Locate malaria parasites and identify their life-cycle stages.
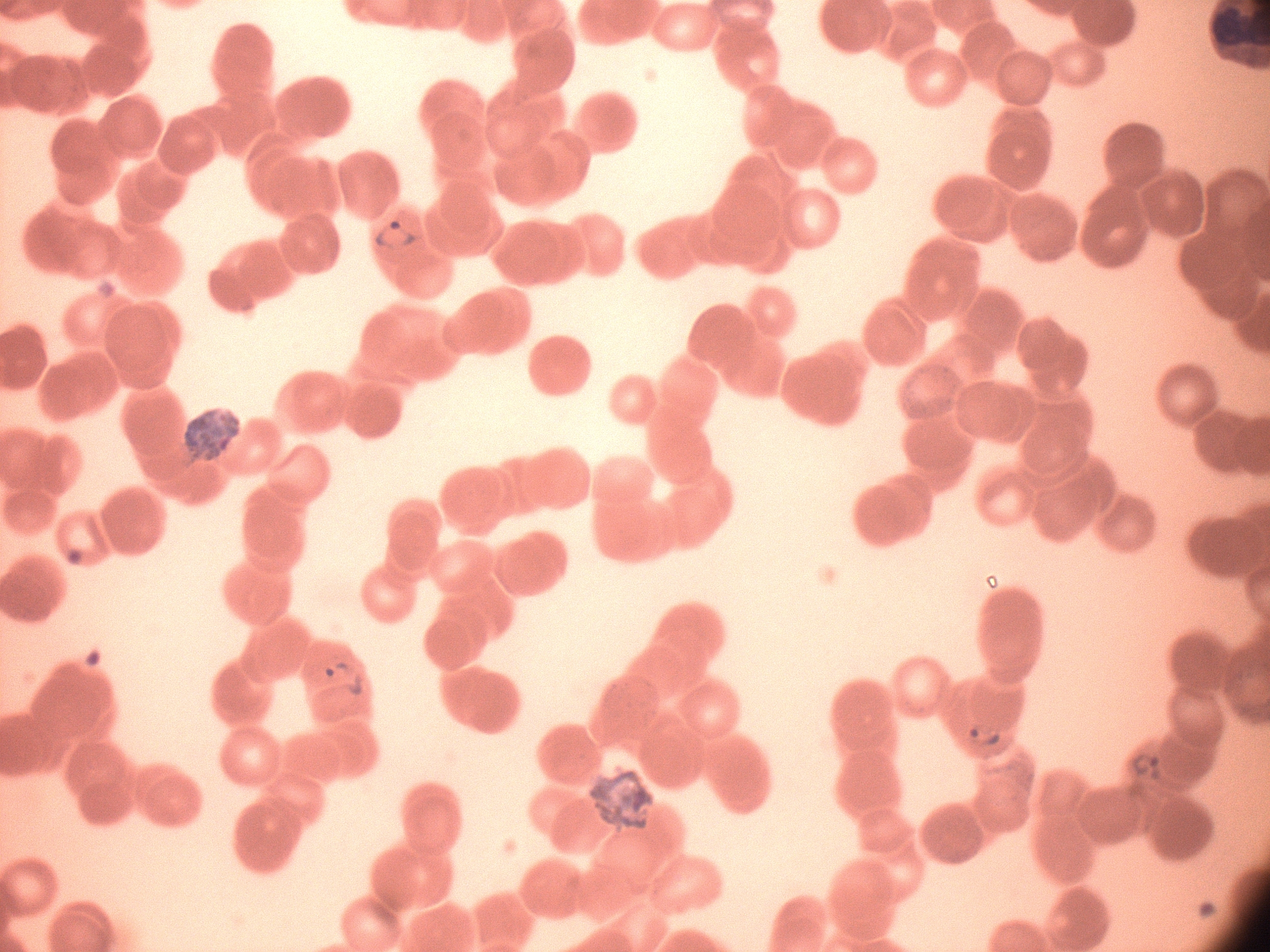
Approximate bounding boxes as [x1, y1, x2, y2] in pixels, from the source annotation, which is not necessarily exhaustive.
Ring forms: [366, 214, 425, 257], [319, 654, 372, 703], [954, 710, 1008, 755], [1119, 740, 1176, 788].

preparation = thin blood film
stain = Giemsa
species = Plasmodium falciparum
microscope = Leica DM2000 with built-in camera
image size = 1270×952 pixels
field of view = one from this slide
magnification = 100x